Assess this cell for malaria.
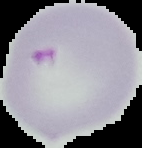

It is parasitized.

Summary:
  - Image size: 142×148 pixels
  - Image type: segmented cell region with the area outside set to black
  - Preparation: thin blood smear